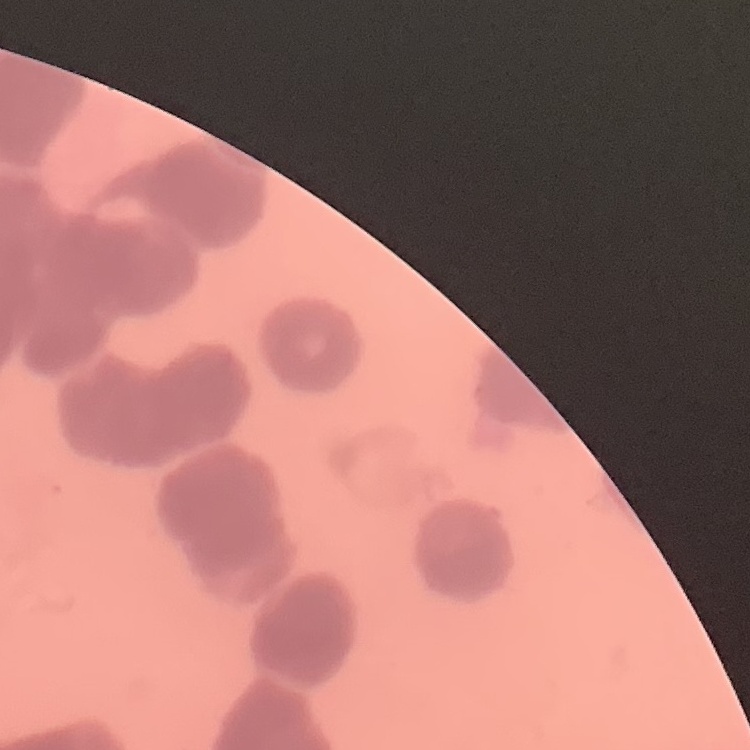 The red blood cells show rouleaux formation. Square crop of a larger photomicrograph. Thin blood smear. Stained with either Field's or Giemsa.